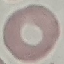

{
  "malaria_status": "uninfected",
  "capture": "smartphone through the microscope eyepiece",
  "preparation": "thin blood smear",
  "stain": "Giemsa",
  "image_type": "automatically extracted cell patch, resized to 64 × 64 pixels"
}